Outline each blood parasite and name the species.
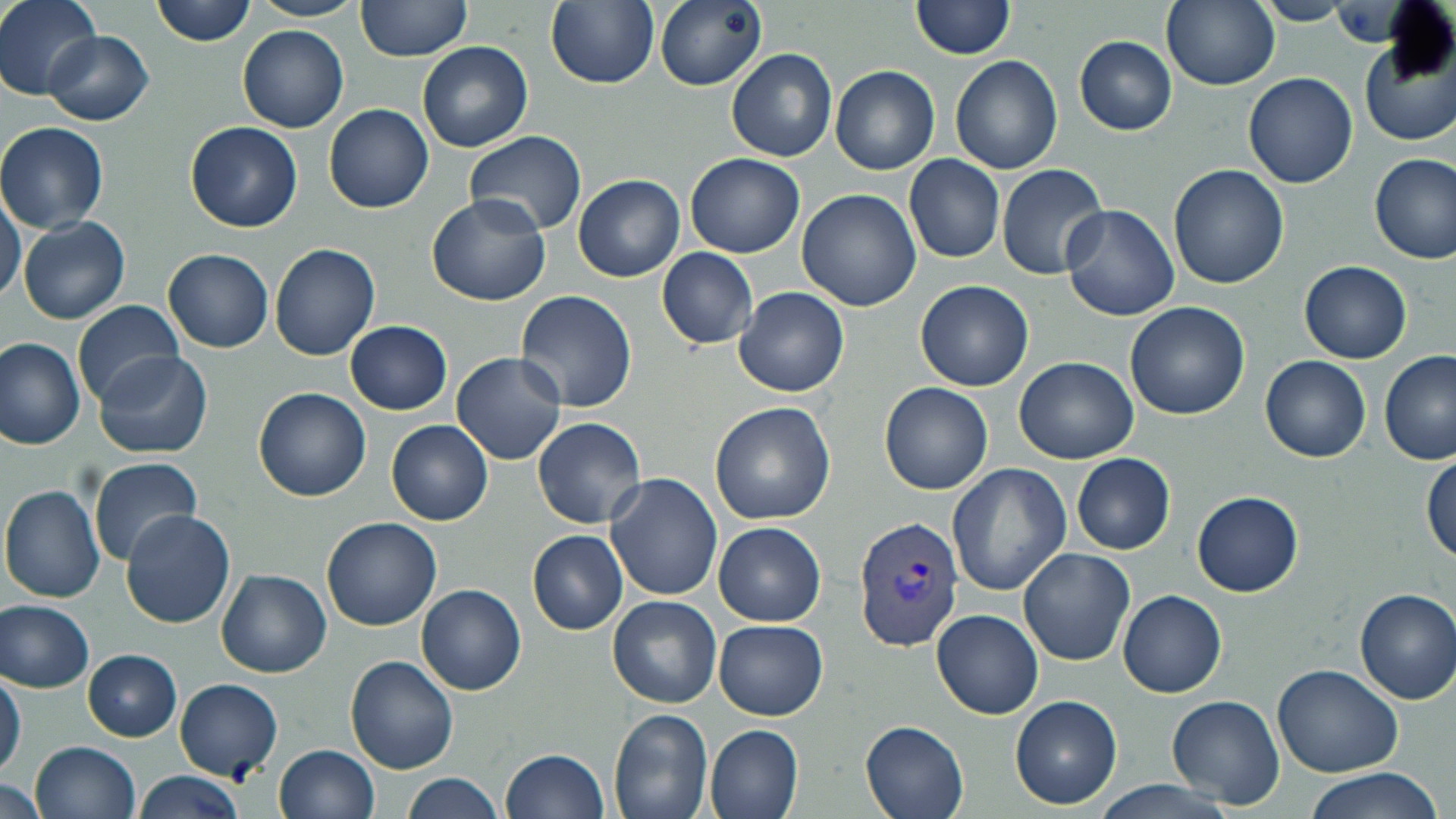

Approximate bounding boxes as named x1/y1/x2/y2 corners in pixels.
Plasmodium vivax-infected red blood cells: (x1=854, y1=514, x2=966, y2=652).
No Plasmodium falciparum, Plasmodium ovale, Plasmodium malariae, Babesia divergens, or Trypanosoma brucei observed.

Uninfected red blood cell locations: (x1=1, y1=0, x2=103, y2=97), (x1=151, y1=0, x2=257, y2=47), (x1=248, y1=0, x2=364, y2=21), (x1=356, y1=0, x2=473, y2=60), (x1=546, y1=0, x2=659, y2=89), (x1=656, y1=0, x2=767, y2=90), (x1=911, y1=0, x2=1015, y2=60), (x1=1161, y1=0, x2=1279, y2=90), (x1=1253, y1=2, x2=1353, y2=25), (x1=237, y1=24, x2=349, y2=130), (x1=44, y1=31, x2=153, y2=126), (x1=1360, y1=31, x2=1456, y2=149), (x1=1076, y1=37, x2=1176, y2=135), (x1=416, y1=40, x2=533, y2=151), (x1=727, y1=49, x2=838, y2=162), (x1=950, y1=55, x2=1064, y2=175), (x1=830, y1=65, x2=939, y2=174), (x1=1244, y1=72, x2=1358, y2=188), (x1=324, y1=103, x2=433, y2=212), (x1=187, y1=121, x2=304, y2=233), (x1=0, y1=122, x2=109, y2=232), (x1=463, y1=129, x2=584, y2=238), (x1=685, y1=152, x2=804, y2=256), (x1=1371, y1=153, x2=1455, y2=263), (x1=903, y1=154, x2=1006, y2=264), (x1=996, y1=163, x2=1108, y2=279), (x1=1169, y1=164, x2=1288, y2=290), (x1=573, y1=175, x2=685, y2=281), (x1=0, y1=188, x2=24, y2=305), (x1=796, y1=188, x2=921, y2=312), (x1=427, y1=194, x2=551, y2=306), (x1=1060, y1=204, x2=1180, y2=322), (x1=18, y1=216, x2=131, y2=324), (x1=270, y1=242, x2=381, y2=360), (x1=656, y1=248, x2=758, y2=349), (x1=160, y1=249, x2=275, y2=351), (x1=1299, y1=260, x2=1411, y2=363), (x1=915, y1=280, x2=1034, y2=391), (x1=734, y1=286, x2=849, y2=397), (x1=515, y1=289, x2=637, y2=412), (x1=73, y1=299, x2=187, y2=404), (x1=1125, y1=302, x2=1248, y2=420), (x1=344, y1=319, x2=451, y2=415), (x1=0, y1=338, x2=85, y2=451), (x1=91, y1=349, x2=214, y2=459), (x1=1378, y1=350, x2=1454, y2=465), (x1=450, y1=352, x2=567, y2=466), (x1=1261, y1=355, x2=1371, y2=461), (x1=1015, y1=356, x2=1137, y2=463), (x1=881, y1=383, x2=993, y2=495), (x1=253, y1=388, x2=371, y2=502), (x1=709, y1=401, x2=836, y2=525), (x1=532, y1=417, x2=647, y2=529), (x1=387, y1=420, x2=494, y2=526), (x1=1071, y1=454, x2=1175, y2=555), (x1=1423, y1=454, x2=1456, y2=562), (x1=88, y1=456, x2=202, y2=563), (x1=946, y1=463, x2=1072, y2=596), (x1=604, y1=475, x2=723, y2=604), (x1=1, y1=484, x2=107, y2=603), (x1=1191, y1=490, x2=1303, y2=597), (x1=120, y1=510, x2=237, y2=628), (x1=322, y1=516, x2=441, y2=630), (x1=715, y1=522, x2=826, y2=625), (x1=528, y1=529, x2=627, y2=634), (x1=1018, y1=546, x2=1135, y2=665), (x1=217, y1=570, x2=331, y2=677), (x1=417, y1=583, x2=527, y2=695), (x1=1117, y1=588, x2=1226, y2=698), (x1=1354, y1=589, x2=1456, y2=703), (x1=608, y1=595, x2=722, y2=708), (x1=0, y1=599, x2=96, y2=693), (x1=933, y1=609, x2=1043, y2=719), (x1=714, y1=620, x2=828, y2=719), (x1=83, y1=650, x2=183, y2=741), (x1=345, y1=655, x2=460, y2=773), (x1=1272, y1=664, x2=1405, y2=780), (x1=0, y1=667, x2=25, y2=780), (x1=175, y1=679, x2=285, y2=781), (x1=1011, y1=694, x2=1121, y2=808), (x1=1167, y1=694, x2=1285, y2=807), (x1=608, y1=709, x2=713, y2=819), (x1=860, y1=717, x2=971, y2=819), (x1=705, y1=722, x2=804, y2=819), (x1=33, y1=742, x2=141, y2=819), (x1=275, y1=744, x2=381, y2=819), (x1=500, y1=747, x2=609, y2=819), (x1=1299, y1=765, x2=1447, y2=819), (x1=135, y1=770, x2=246, y2=819), (x1=402, y1=771, x2=507, y2=819), (x1=0, y1=777, x2=48, y2=819), (x1=1083, y1=780, x2=1245, y2=819). Slide-level diagnosis: Plasmodium vivax. Single field of view. May-Grünwald-Giemsa-stained preparation. Captured at 1000x magnification. Light microscopy. Image is 1456×819 pixels. Thin blood smear.